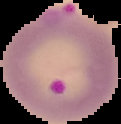

image type = cell region segmented out of the field of view; surrounding area masked to black
image size = 121×124 pixels
malaria status = parasitized
preparation = thin blood film